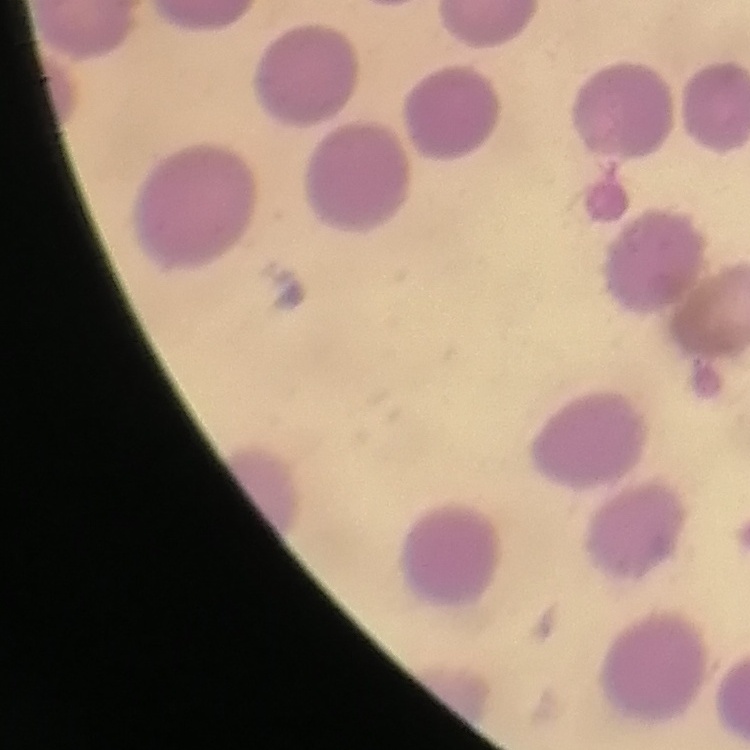

Summary:
  - Red blood cell morphology: no rouleaux formation
  - Stain: Field's or Giemsa
  - Preparation: thin peripheral smear
  - Image type: square crop of a larger photomicrograph